Name the blood parasite species.
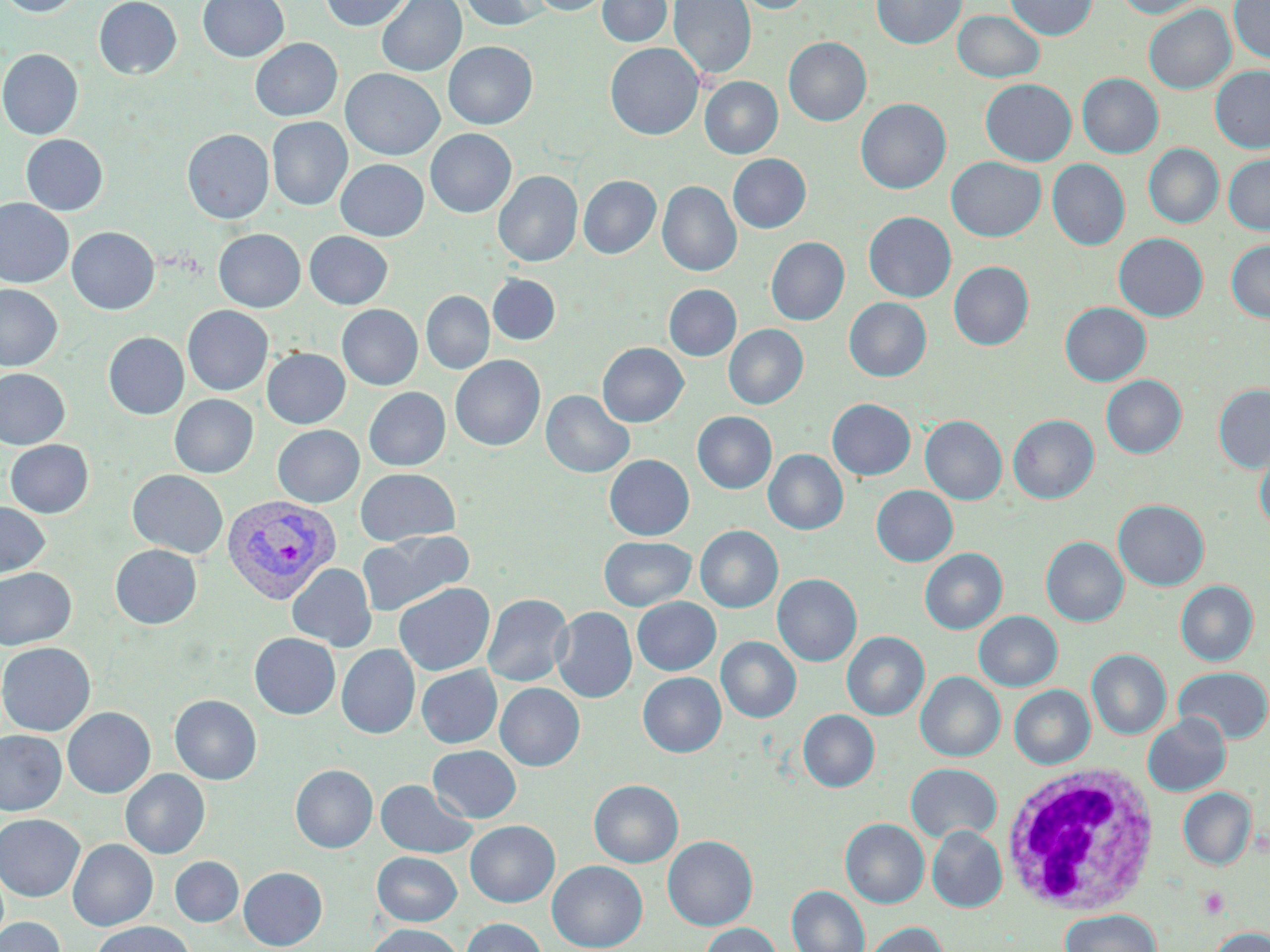
Plasmodium vivax.

Approximate bounding boxes as (x1, y1, x2, y2) in pixels. Platelet locations: (1198, 887, 1229, 919). Uninfected red blood cell locations: (1, 0, 85, 17), (94, 0, 182, 79), (198, 0, 288, 62), (321, 0, 412, 31), (377, 0, 466, 76), (458, 0, 550, 31), (529, 0, 612, 15), (597, 0, 672, 47), (669, 0, 756, 80), (734, 0, 813, 14), (872, 0, 966, 50), (1005, 0, 1098, 39), (1116, 0, 1207, 18), (1229, 0, 1270, 63), (1144, 5, 1236, 94), (952, 10, 1046, 82), (783, 37, 871, 126), (250, 38, 343, 121), (443, 41, 537, 129), (605, 43, 704, 140), (0, 48, 83, 140), (1210, 65, 1270, 153), (341, 69, 443, 159), (1077, 73, 1163, 158), (700, 76, 782, 159), (980, 78, 1076, 166), (855, 98, 951, 194), (267, 117, 352, 210), (182, 129, 274, 224), (425, 129, 516, 217), (21, 134, 108, 215), (1143, 143, 1224, 228), (1223, 153, 1270, 235), (728, 154, 811, 233), (946, 156, 1046, 241), (336, 159, 428, 240), (1047, 159, 1130, 250), (494, 171, 582, 266), (578, 176, 660, 258), (657, 181, 741, 277), (0, 199, 74, 288), (863, 211, 956, 302), (67, 226, 159, 314), (213, 229, 305, 312), (304, 231, 393, 309), (1113, 233, 1208, 321), (766, 237, 849, 325), (1226, 240, 1270, 322), (948, 261, 1034, 350), (487, 274, 560, 345), (0, 284, 63, 371), (663, 284, 741, 361), (421, 291, 494, 374), (844, 298, 931, 381), (1060, 302, 1151, 385), (337, 304, 422, 390), (183, 305, 273, 395), (724, 324, 808, 409), (104, 332, 189, 419), (598, 342, 688, 427), (262, 348, 350, 428), (450, 355, 545, 451), (0, 368, 70, 449), (1101, 375, 1186, 458), (1213, 384, 1270, 473), (364, 387, 450, 471), (541, 390, 634, 478), (170, 394, 258, 478), (827, 399, 915, 480), (693, 411, 777, 493), (920, 415, 1007, 505), (1008, 415, 1099, 504), (273, 425, 364, 507), (4, 440, 94, 518), (1255, 447, 1270, 533), (764, 449, 848, 535), (604, 454, 694, 540), (355, 468, 460, 546), (128, 470, 228, 558), (871, 485, 958, 567), (1113, 499, 1209, 590), (0, 501, 50, 580), (695, 525, 783, 612), (359, 530, 473, 616), (599, 536, 695, 610), (1041, 536, 1128, 627), (110, 544, 202, 629), (920, 548, 1007, 634), (287, 563, 376, 652), (0, 567, 76, 650), (773, 574, 862, 667), (1176, 580, 1258, 666), (393, 582, 494, 676), (483, 593, 572, 687), (632, 597, 720, 675), (551, 606, 637, 702), (974, 611, 1062, 691), (842, 631, 929, 720), (249, 633, 340, 719), (716, 636, 801, 722), (0, 642, 96, 735), (336, 644, 420, 739), (1086, 648, 1171, 740), (416, 665, 502, 748), (1173, 666, 1270, 744), (638, 672, 726, 756), (916, 672, 1005, 761), (495, 682, 584, 770), (1010, 685, 1095, 769), (170, 695, 262, 784), (62, 707, 155, 798), (798, 709, 879, 792), (1143, 714, 1231, 796), (0, 730, 66, 815), (428, 745, 521, 823), (906, 763, 1001, 843), (290, 764, 378, 852), (121, 769, 209, 858), (375, 779, 477, 858), (589, 779, 683, 867), (1178, 787, 1256, 870), (0, 814, 85, 901), (840, 818, 929, 908), (465, 820, 560, 906), (927, 826, 1007, 912), (663, 835, 757, 930), (68, 839, 158, 930), (372, 852, 461, 925), (170, 856, 243, 926), (169, 859, 325, 930), (547, 860, 647, 951), (238, 866, 327, 949), (787, 885, 869, 952), (1060, 909, 1160, 952), (0, 916, 65, 952), (460, 918, 547, 952), (92, 921, 196, 952), (863, 922, 948, 952), (700, 923, 781, 952), (364, 924, 466, 952), (1209, 927, 1270, 952). White blood cell locations: (999, 763, 1160, 917). Plasmodium vivax-infected red blood cell locations: (221, 495, 341, 604). Captured at 1000x magnification. Single field of view. May-Grünwald-Giemsa stain. Thin blood film. Image is 1270×952 pixels. Optical microscopy.